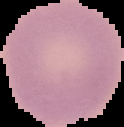

Summary:
  - Image size: 124×127 pixels
  - Image type: segmented cell region on a black background
  - Result: no malaria parasites detected
  - Preparation: thin blood smear